Give the position of every leukocyte visible.
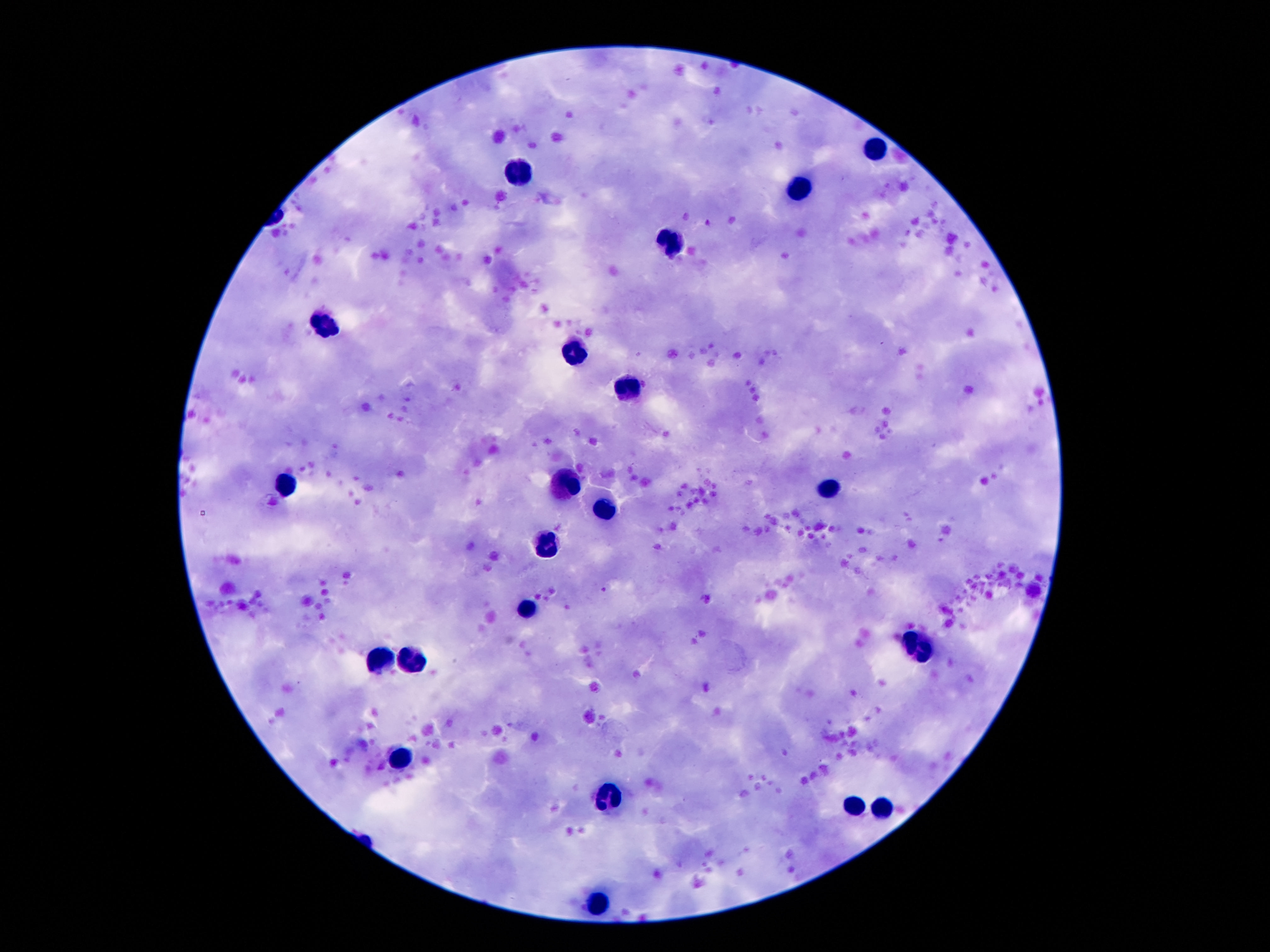
Approximate centers as [x, y] in pixels.
Leukocytes: [872, 149], [521, 174], [800, 191], [674, 243], [324, 325], [574, 352], [630, 386], [568, 483], [286, 485], [828, 491], [607, 508], [547, 544], [528, 611], [914, 643], [383, 658], [412, 660], [402, 760], [609, 796], [853, 807], [882, 811], [597, 906].

field of view = one from this slide
image size = 1270×952 pixels
stain = Giemsa
capture = smartphone camera through the microscope eyepiece
magnification = 100x
patient malaria status = uninfected
preparation = thick peripheral-blood smear